Describe the morphology of the red blood cells.
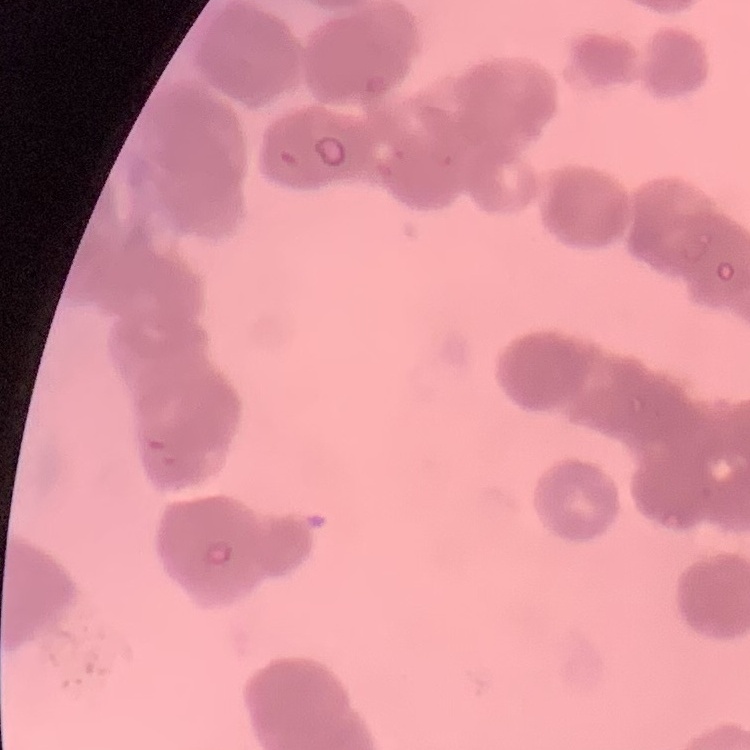

Rouleaux formation.

Thin blood smear. One tile cut from a larger photomicrograph. Field's or Giemsa stain.